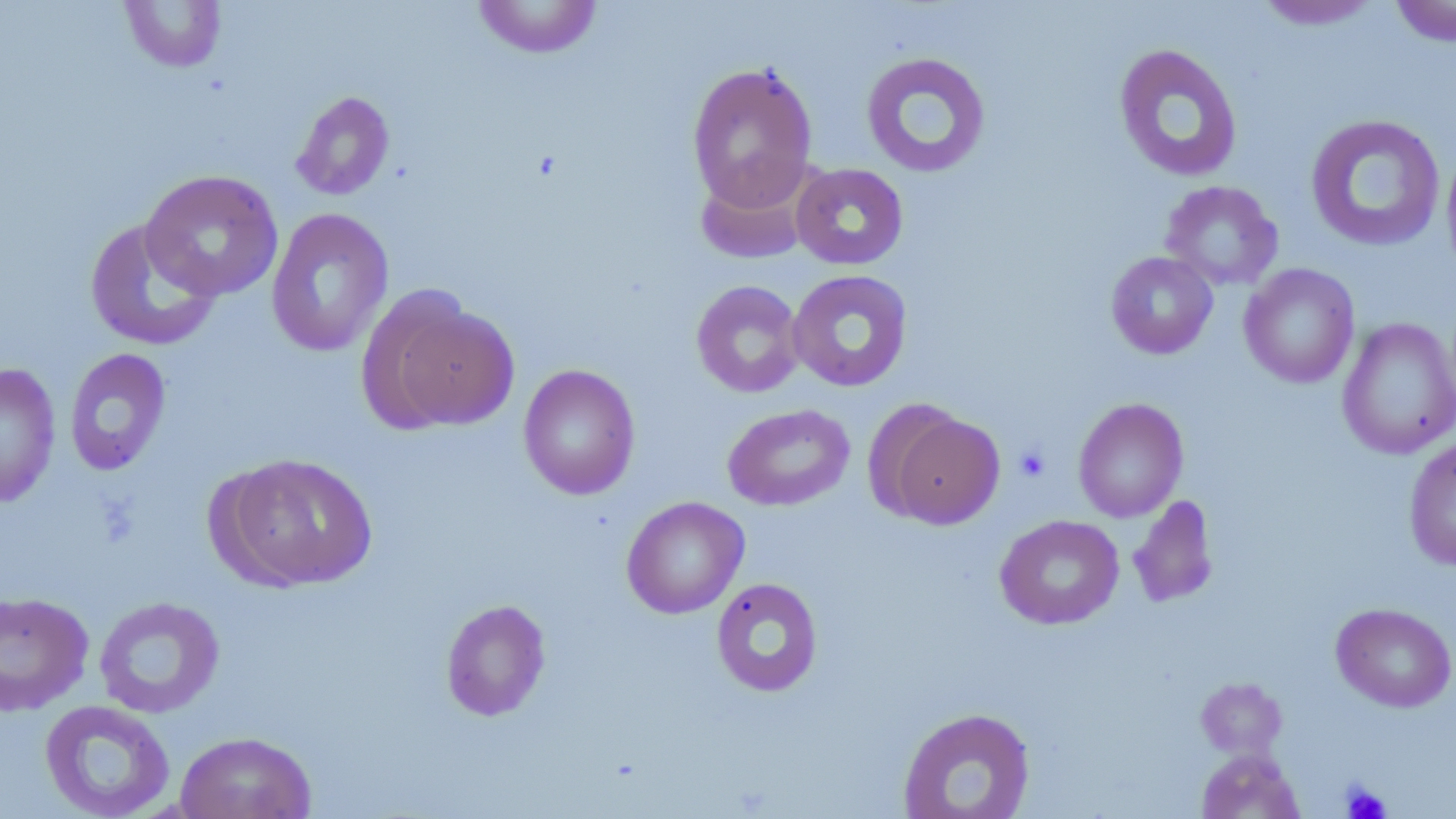 Approximate bounding boxes as (x1, y1, x2, y2) in pixels. Uninfected red blood cell locations: (471, 0, 604, 59), (1389, 0, 1456, 47), (120, 1, 227, 73), (1252, 1, 1384, 31), (1113, 42, 1243, 183), (860, 51, 991, 179), (686, 61, 818, 211), (290, 90, 395, 201), (1304, 113, 1446, 253), (1441, 144, 1456, 279), (791, 162, 909, 270), (697, 163, 814, 265), (139, 169, 285, 302), (1160, 180, 1283, 291), (266, 207, 394, 357), (84, 218, 222, 352), (1105, 251, 1218, 360), (1239, 263, 1360, 389), (786, 269, 913, 392), (691, 280, 805, 398), (379, 299, 518, 432), (1336, 317, 1456, 460), (63, 347, 172, 477), (0, 361, 61, 508), (518, 364, 640, 500), (1073, 397, 1189, 523), (722, 403, 855, 510), (884, 409, 1004, 529), (1403, 437, 1456, 571), (219, 452, 379, 591), (1127, 495, 1219, 609), (621, 496, 749, 619), (995, 514, 1124, 630), (711, 578, 824, 697), (0, 590, 94, 716), (93, 596, 226, 718), (440, 599, 551, 721), (1331, 603, 1456, 712), (1195, 677, 1291, 761), (39, 700, 176, 819), (897, 707, 1036, 818), (175, 731, 317, 819), (1196, 748, 1305, 819). Platelet locations: (1014, 444, 1051, 483), (1339, 781, 1392, 819). Slide-level diagnosis: no evidence of blood parasites. 1000x magnification. One field of a larger specimen. Thin blood film. May-Grünwald-Giemsa stain. Image is 1456×819 pixels. Light microscopy.